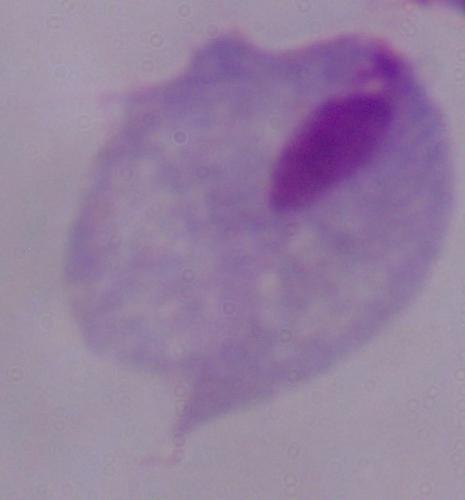
magnification = 1000x
modality = micrograph
identification = trichomonad